Identify the parasite.
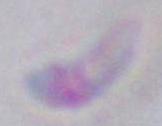

This is Toxoplasma gondii.

Summary:
  - Magnification: 1000x
  - Modality: photomicrograph